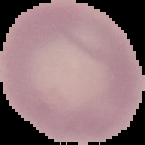 Image is 145×145 pixels. Malaria status: uninfected. From a thin blood smear. The area outside the segmented cell region is set to black.